Give a bounding box for every parasitised red blood cell.
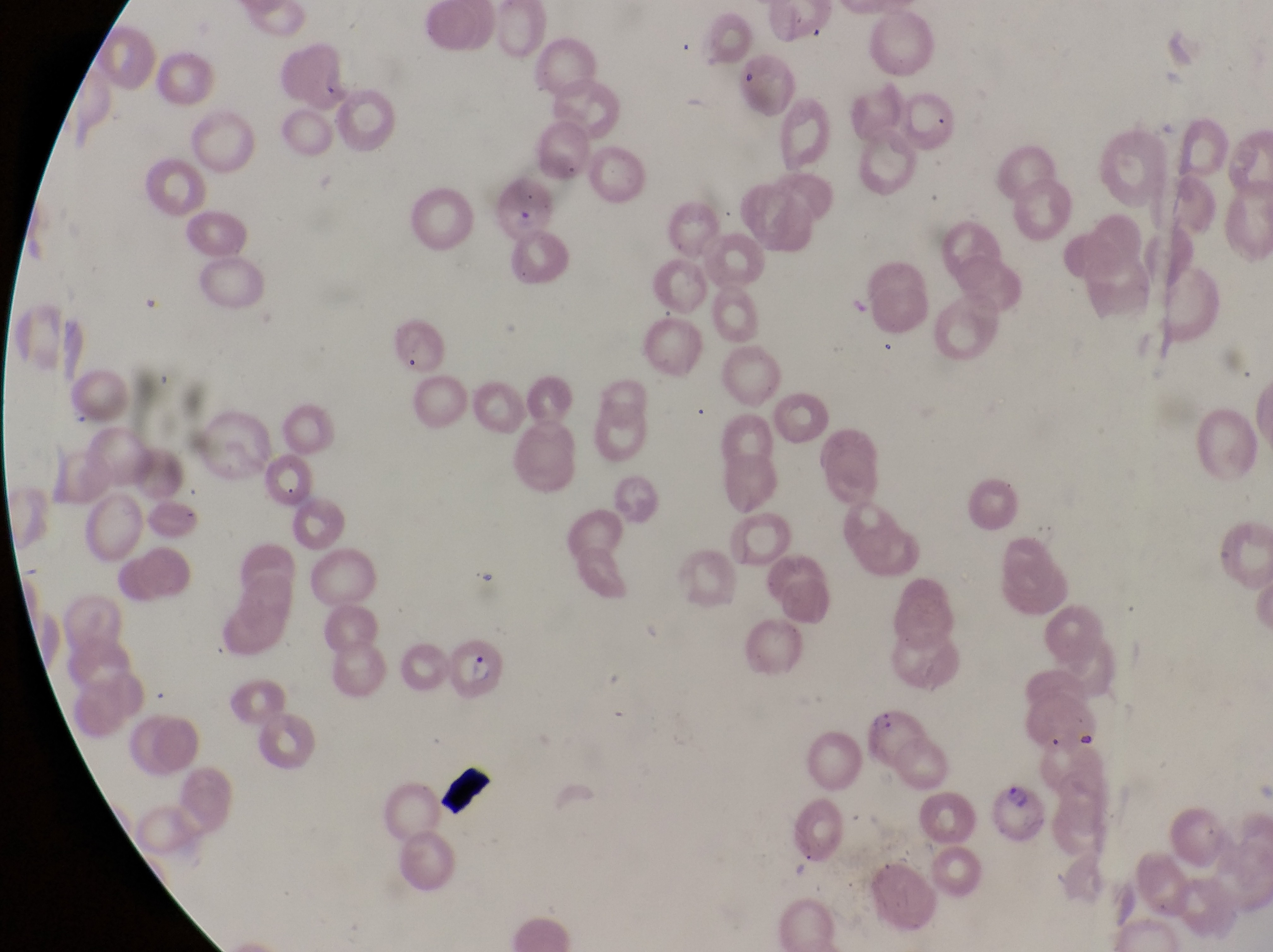

Approximate bounding boxes as [left, top, right, bottom] in pixels.
Parasitised red blood cells: [486, 167, 558, 239], [391, 312, 448, 375], [452, 639, 509, 702], [864, 705, 922, 762], [996, 781, 1053, 848].

At a magnification of 1000x. Sample from Uganda. Photographed through the eyepiece of an Olympus CX-23 microscope with a smartphone camera. Single field of view. Thin blood film. Image is 1273×952 pixels.